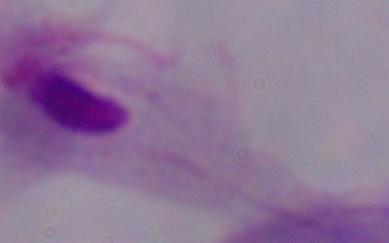

modality = micrograph
identification = trichomonad
magnification = 1000x